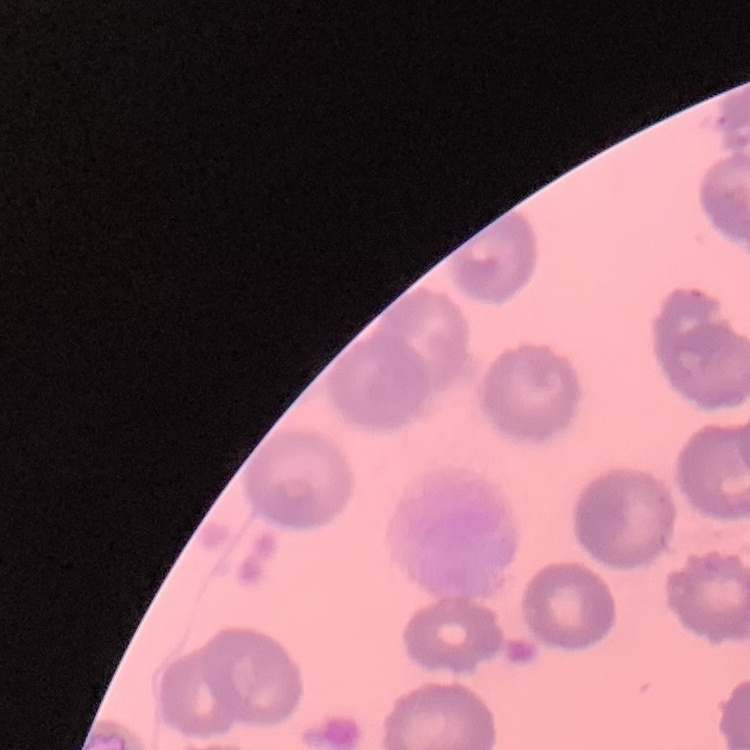

The erythrocytes exhibit no rouleaux formation. Field's or Giemsa stain. Thin blood smear. One tile cut from a larger photomicrograph.